Comment on the morphology of the erythrocytes.
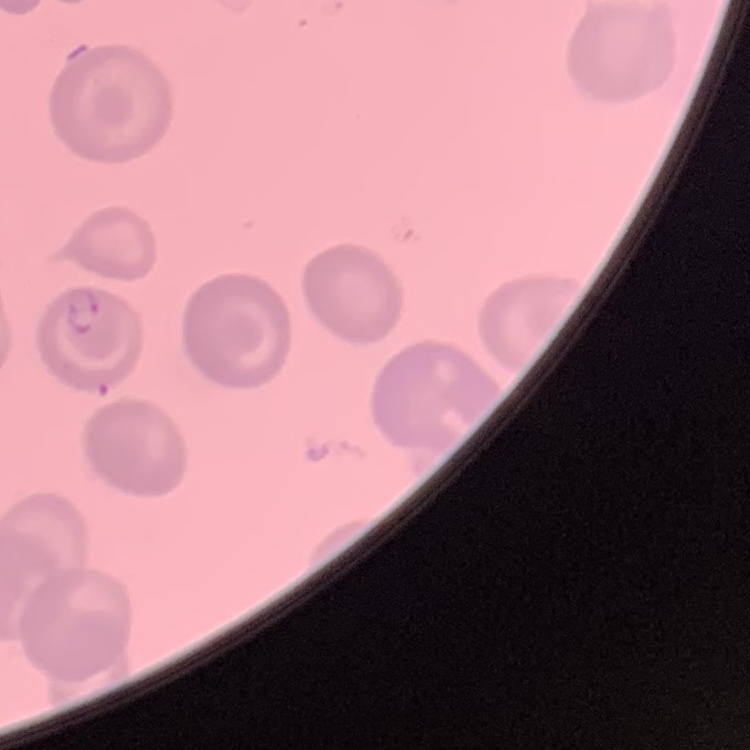

No rouleaux formation.

Field's or Giemsa stain. Thin peripheral smear. One tile cut from a larger photomicrograph.